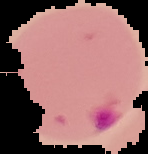
Summary:
  - Image size: 148×154 pixels
  - Preparation: thin blood smear
  - Result: Plasmodium parasites detected
  - Image type: cell region segmented out of the field of view; surrounding area masked to black